Locate every uninfected red blood cell.
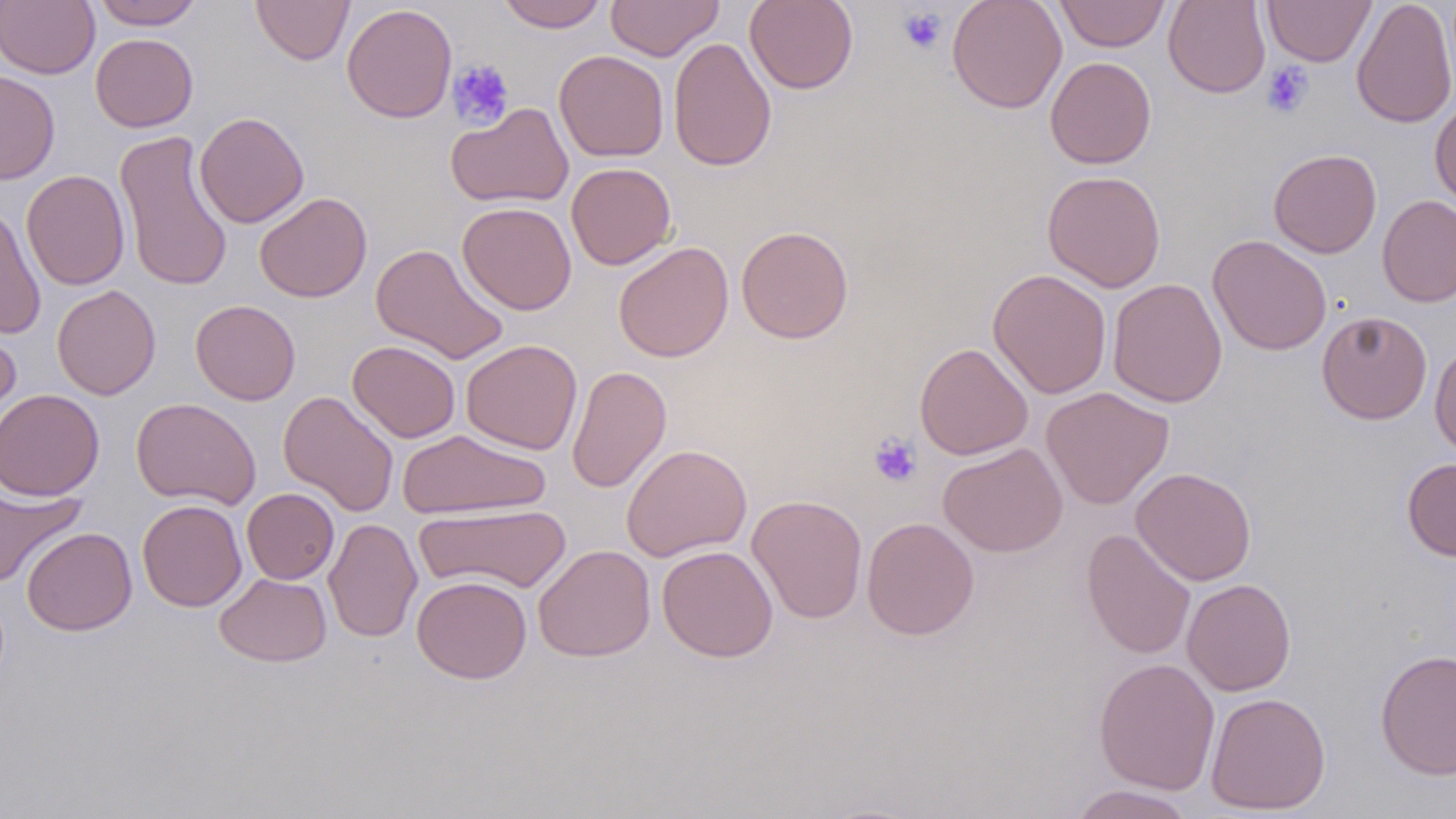
Approximate bounding boxes as [x1, y1, x2, y2] in pixels.
Uninfected red blood cells: [91, 0, 203, 29], [250, 0, 355, 65], [496, 0, 609, 32], [606, 0, 723, 60], [745, 0, 858, 94], [946, 0, 1067, 113], [1054, 0, 1171, 52], [1163, 0, 1271, 98], [1263, 0, 1376, 66], [1351, 0, 1456, 129], [0, 1, 99, 79], [341, 3, 457, 122], [91, 33, 198, 132], [668, 37, 776, 172], [554, 50, 669, 162], [1045, 56, 1156, 169], [0, 69, 60, 184], [1430, 98, 1456, 209], [446, 102, 573, 208], [194, 112, 309, 228], [114, 129, 234, 293], [1268, 149, 1382, 258], [566, 162, 677, 270], [21, 169, 130, 290], [1042, 170, 1166, 292], [254, 192, 372, 302], [1377, 194, 1456, 307], [458, 202, 577, 315], [0, 206, 46, 339], [736, 225, 854, 343], [1207, 234, 1332, 355], [613, 241, 734, 362], [370, 242, 509, 364], [988, 269, 1112, 398], [1107, 278, 1227, 407], [52, 284, 161, 400], [190, 299, 301, 405], [1317, 310, 1432, 424], [0, 321, 21, 441], [461, 339, 583, 454], [347, 340, 461, 443], [1429, 341, 1456, 459], [914, 342, 1034, 460], [567, 365, 671, 493], [1041, 386, 1175, 509], [0, 389, 105, 501], [278, 390, 399, 517], [131, 397, 261, 510], [397, 429, 551, 519], [938, 442, 1067, 557], [621, 443, 752, 561], [1402, 458, 1456, 561], [1131, 467, 1257, 586], [0, 482, 86, 589], [242, 488, 339, 584], [748, 494, 868, 624], [137, 499, 247, 611], [414, 502, 573, 595], [324, 517, 422, 643], [861, 517, 979, 640], [22, 527, 136, 635], [1081, 528, 1196, 660], [533, 544, 655, 662], [657, 545, 778, 662], [214, 573, 331, 667], [412, 575, 531, 684], [1182, 578, 1296, 696], [1375, 649, 1456, 781], [1093, 657, 1220, 795], [1205, 692, 1331, 814], [1066, 784, 1197, 818].

Platelet locations: [898, 7, 946, 55], [447, 59, 515, 131], [1262, 61, 1314, 118], [868, 433, 922, 487]. Slide-level diagnosis: negative for blood parasites. Image is 1456×819 pixels. Thin blood smear. May-Grünwald-Giemsa stain. Optical microscopy. Captured at 1000x magnification. One field of a larger specimen.